Classify the preparation.
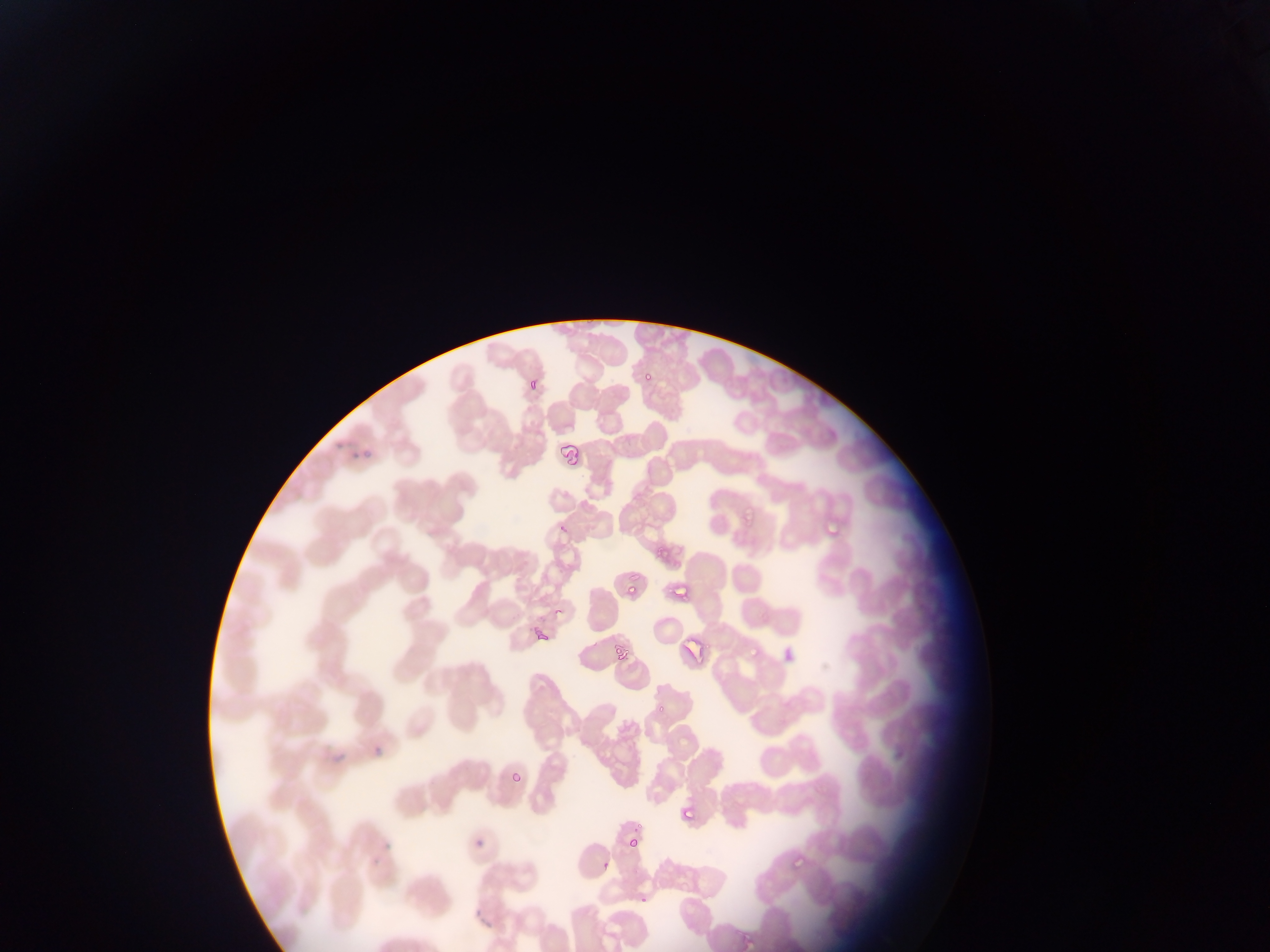
Thin blood smear.

Approximate bounding boxes as left top right bottom in pixels. Plasmodium parasite locations: 522 365 548 389; 640 370 658 384; 556 441 588 468; 741 503 762 523; 823 524 843 537; 669 572 700 607; 620 573 638 593; 548 593 568 620; 749 630 772 653; 606 635 637 670; 655 691 678 719; 506 766 529 792; 676 801 703 831; 625 835 642 848; 781 852 804 870; 599 858 616 876. Single field of view. Photographed through a microscope with a mobile-phone camera. Image is 1270×952 pixels. Collected in Ghana.